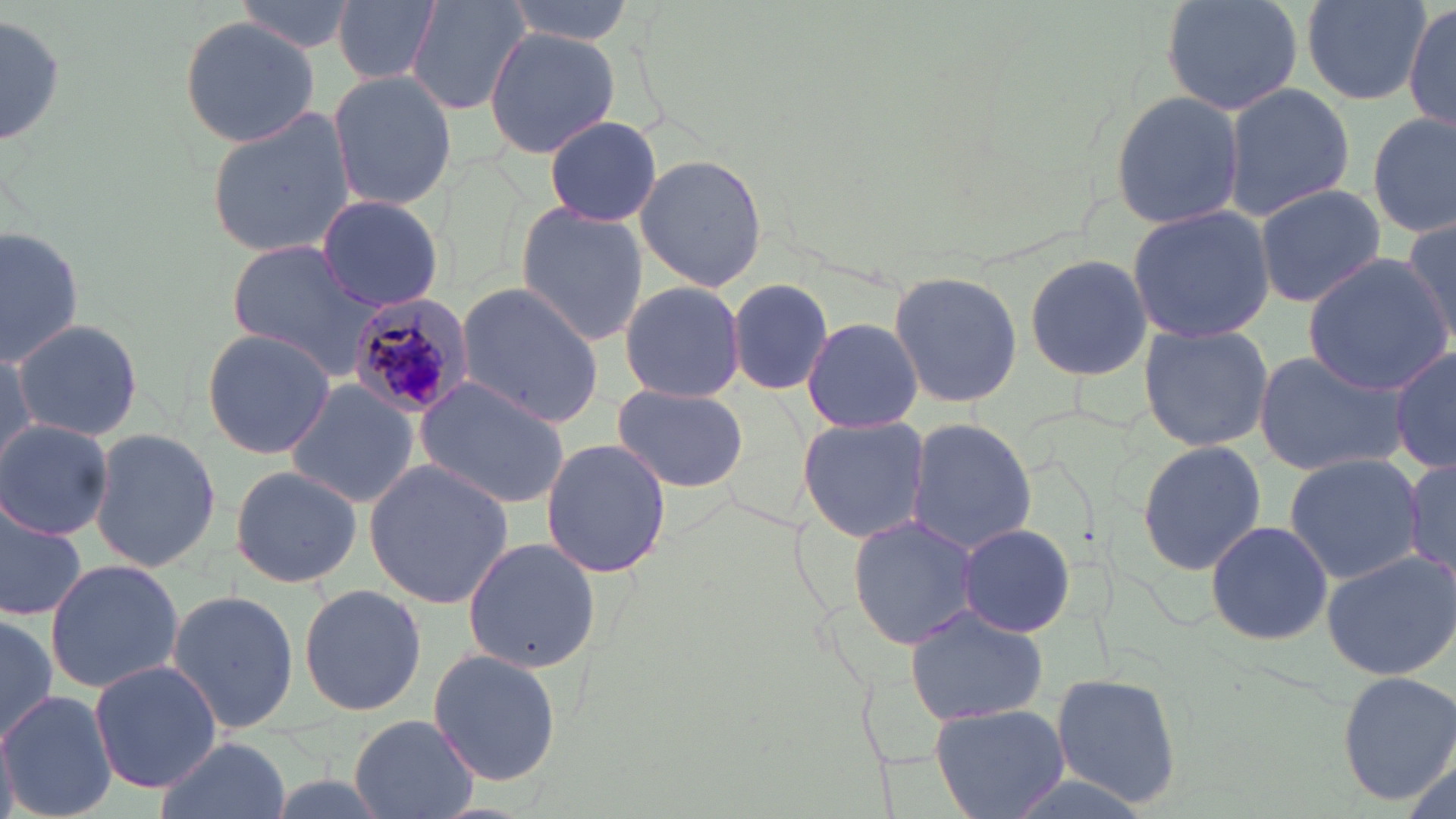 Approximate bounding boxes as (x1, y1, x2, y2) in pixels. Uninfected red blood cell locations: (334, 0, 439, 86), (407, 0, 530, 117), (501, 0, 635, 43), (1162, 0, 1302, 113), (1298, 0, 1433, 106), (232, 3, 359, 52), (1401, 4, 1455, 133), (2, 11, 64, 154), (178, 17, 319, 150), (483, 24, 623, 158), (328, 69, 454, 211), (1222, 83, 1355, 219), (1107, 90, 1246, 232), (203, 107, 357, 260), (1369, 108, 1455, 239), (544, 114, 663, 227), (634, 154, 769, 290), (1252, 184, 1387, 309), (316, 195, 444, 311), (514, 202, 650, 347), (1127, 204, 1276, 344), (1402, 217, 1456, 350), (0, 225, 82, 360), (222, 239, 389, 377), (1022, 253, 1154, 384), (1301, 254, 1453, 394), (885, 270, 1023, 409), (724, 279, 833, 397), (619, 280, 745, 403), (455, 281, 605, 427), (802, 317, 923, 432), (11, 318, 145, 444), (1138, 323, 1275, 453), (200, 328, 335, 460), (0, 343, 35, 470), (1389, 345, 1456, 474), (1251, 347, 1410, 479), (412, 375, 571, 509), (284, 381, 419, 509), (611, 383, 749, 494), (798, 417, 929, 541), (907, 418, 1036, 554), (0, 420, 114, 539), (87, 427, 221, 574), (540, 437, 673, 579), (1136, 440, 1267, 576), (1282, 453, 1425, 583), (363, 456, 516, 610), (1404, 457, 1456, 580), (229, 465, 364, 588), (0, 498, 87, 620), (848, 515, 982, 649), (1204, 520, 1333, 646), (957, 524, 1078, 637), (463, 538, 600, 671), (1320, 549, 1456, 680), (43, 559, 185, 692), (298, 584, 428, 717), (166, 589, 300, 733), (903, 604, 1049, 730), (0, 610, 58, 752), (428, 648, 563, 788), (89, 661, 222, 793), (1049, 670, 1185, 808), (1337, 670, 1456, 805), (0, 689, 117, 819), (932, 702, 1068, 818), (348, 713, 478, 819), (152, 736, 293, 819). Plasmodium malariae-infected red blood cell locations: (347, 293, 475, 422). Slide-level diagnosis: Plasmodium malariae. Light microscopy. One field of a larger specimen. Image is 1456×819 pixels. Thin blood smear. 1000x magnification. May-Grünwald-Giemsa stain.